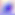
Summary:
  - Identification: Toxoplasma gondii
  - Modality: photomicrograph
  - Magnification: 400x